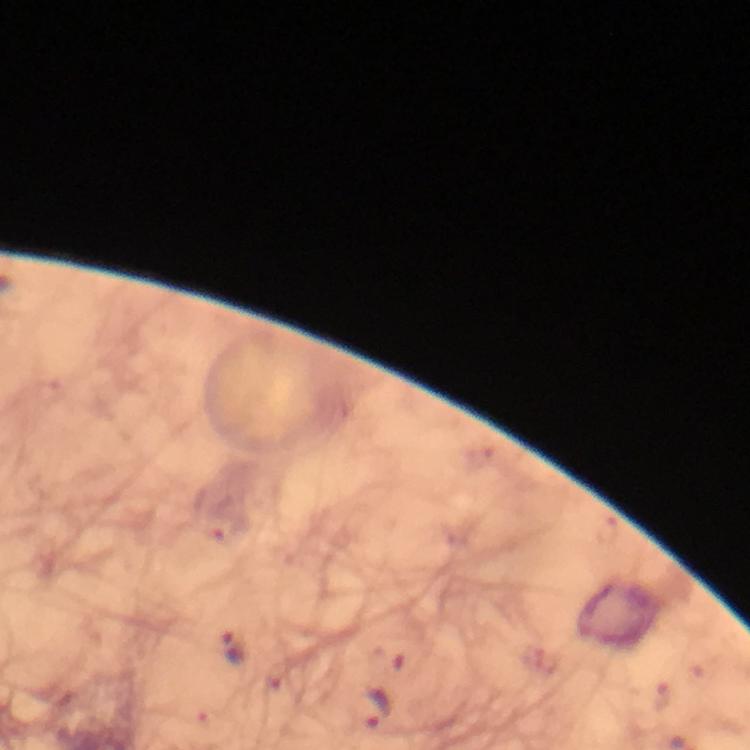
Approximate centers as {x, y} in pixels.
Summary:
  - Plasmodium parasite locations: {233, 649}, {376, 709}
  - Cropped from: a single field of view
  - Capture: smartphone camera through the microscope
  - Preparation: thick blood film
  - Context: from a diagnostic examination for malaria
  - Stain: Giemsa
  - Image size: 750×750 pixels
  - Immersion oil: applied
  - Magnification: 100x